State the blood parasite species.
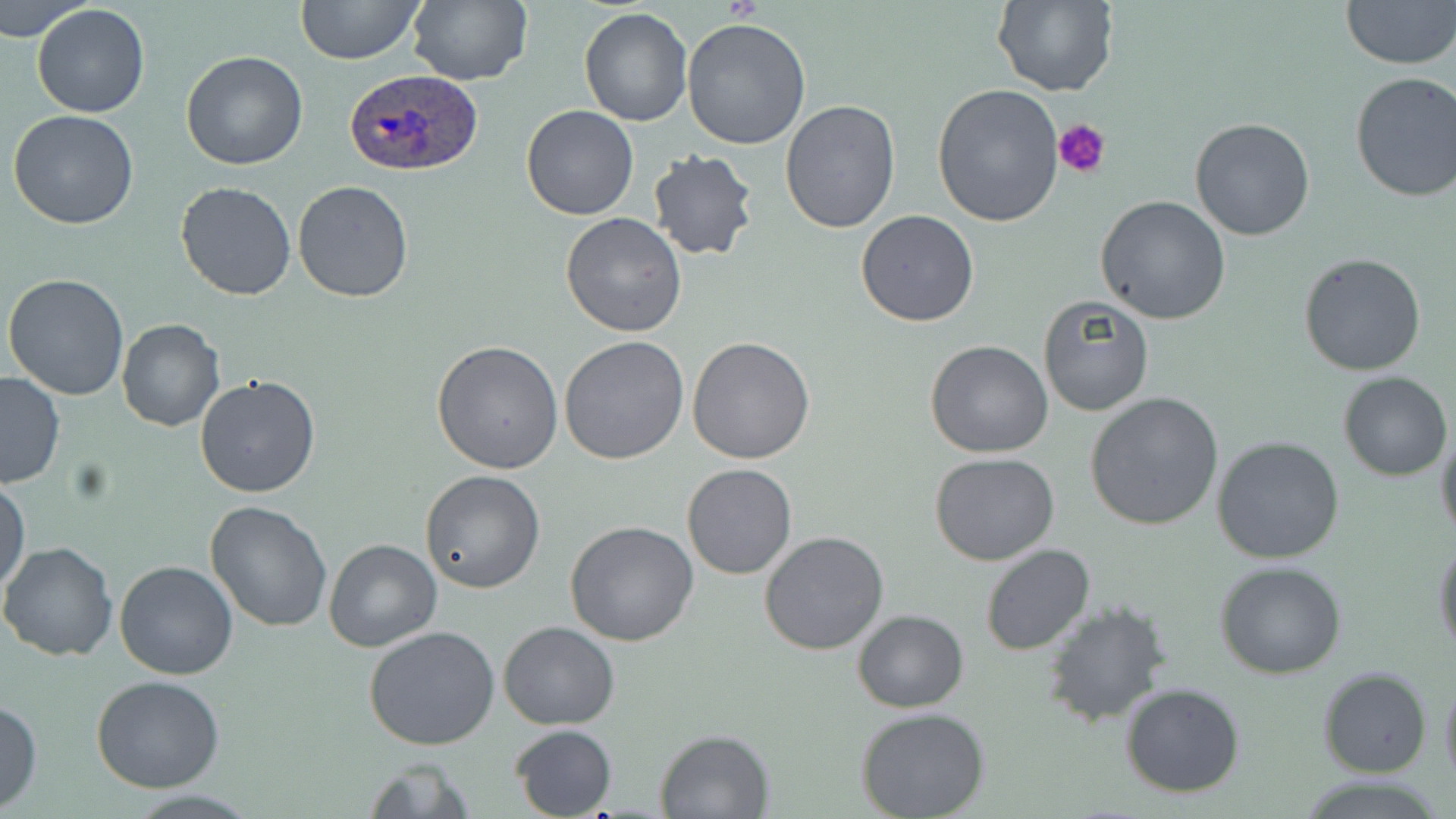

Plasmodium ovale.

Approximate bounding boxes as named x1/y1/x2/y2 corners in pixels. Platelet locations: (x1=1054, y1=119, x2=1113, y2=179). Plasmodium ovale-infected red blood cell locations: (x1=342, y1=68, x2=482, y2=179). Uninfected red blood cell locations: (x1=1, y1=0, x2=92, y2=40), (x1=295, y1=0, x2=423, y2=64), (x1=406, y1=0, x2=531, y2=85), (x1=991, y1=0, x2=1117, y2=96), (x1=1340, y1=0, x2=1454, y2=69), (x1=32, y1=2, x2=151, y2=118), (x1=579, y1=8, x2=694, y2=127), (x1=681, y1=18, x2=810, y2=149), (x1=180, y1=49, x2=309, y2=170), (x1=1349, y1=71, x2=1456, y2=203), (x1=931, y1=83, x2=1063, y2=228), (x1=780, y1=98, x2=901, y2=233), (x1=520, y1=104, x2=638, y2=220), (x1=8, y1=109, x2=140, y2=229), (x1=1190, y1=117, x2=1314, y2=242), (x1=645, y1=150, x2=760, y2=261), (x1=174, y1=180, x2=298, y2=301), (x1=293, y1=181, x2=415, y2=302), (x1=1095, y1=195, x2=1231, y2=324), (x1=857, y1=211, x2=979, y2=328), (x1=560, y1=213, x2=688, y2=338), (x1=1298, y1=251, x2=1427, y2=375), (x1=3, y1=274, x2=130, y2=400), (x1=1037, y1=295, x2=1154, y2=417), (x1=117, y1=319, x2=225, y2=434), (x1=687, y1=335, x2=816, y2=464), (x1=559, y1=336, x2=690, y2=466), (x1=432, y1=340, x2=564, y2=474), (x1=926, y1=340, x2=1054, y2=458), (x1=1337, y1=372, x2=1451, y2=480), (x1=0, y1=373, x2=66, y2=488), (x1=195, y1=376, x2=322, y2=499), (x1=1084, y1=392, x2=1224, y2=530), (x1=1436, y1=430, x2=1456, y2=547), (x1=1212, y1=436, x2=1345, y2=564), (x1=930, y1=452, x2=1059, y2=565), (x1=682, y1=464, x2=797, y2=580), (x1=421, y1=470, x2=545, y2=593), (x1=0, y1=477, x2=29, y2=595), (x1=204, y1=500, x2=333, y2=632), (x1=564, y1=520, x2=699, y2=647), (x1=759, y1=531, x2=888, y2=655), (x1=1432, y1=537, x2=1455, y2=659), (x1=324, y1=538, x2=442, y2=652), (x1=0, y1=541, x2=120, y2=661), (x1=980, y1=544, x2=1097, y2=657), (x1=115, y1=559, x2=238, y2=681), (x1=1215, y1=560, x2=1347, y2=679), (x1=1041, y1=602, x2=1172, y2=727), (x1=852, y1=609, x2=969, y2=712), (x1=499, y1=620, x2=619, y2=729), (x1=364, y1=626, x2=501, y2=750), (x1=1318, y1=667, x2=1432, y2=778), (x1=1439, y1=670, x2=1456, y2=793), (x1=91, y1=675, x2=225, y2=791), (x1=1120, y1=682, x2=1245, y2=798), (x1=0, y1=698, x2=43, y2=812), (x1=857, y1=709, x2=990, y2=819), (x1=510, y1=724, x2=618, y2=818), (x1=655, y1=729, x2=773, y2=817), (x1=356, y1=759, x2=478, y2=817). One field of a larger specimen. Optical microscopy. Thin blood smear. Captured at 1000x magnification. May-Grünwald-Giemsa-stained preparation. Image is 1456×819 pixels.